State which parasite is depicted.
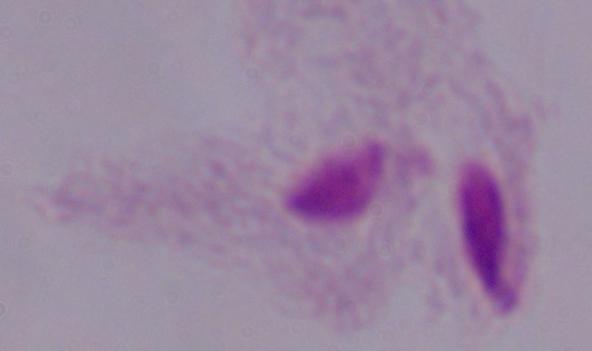
A trichomonad.

Summary:
  - Modality: micrograph
  - Magnification: 1000x